Identify the parasite.
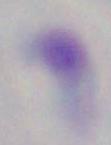
This is Toxoplasma gondii.

Summary:
  - Modality: photomicrograph
  - Magnification: 1000x